Evaluate for malaria.
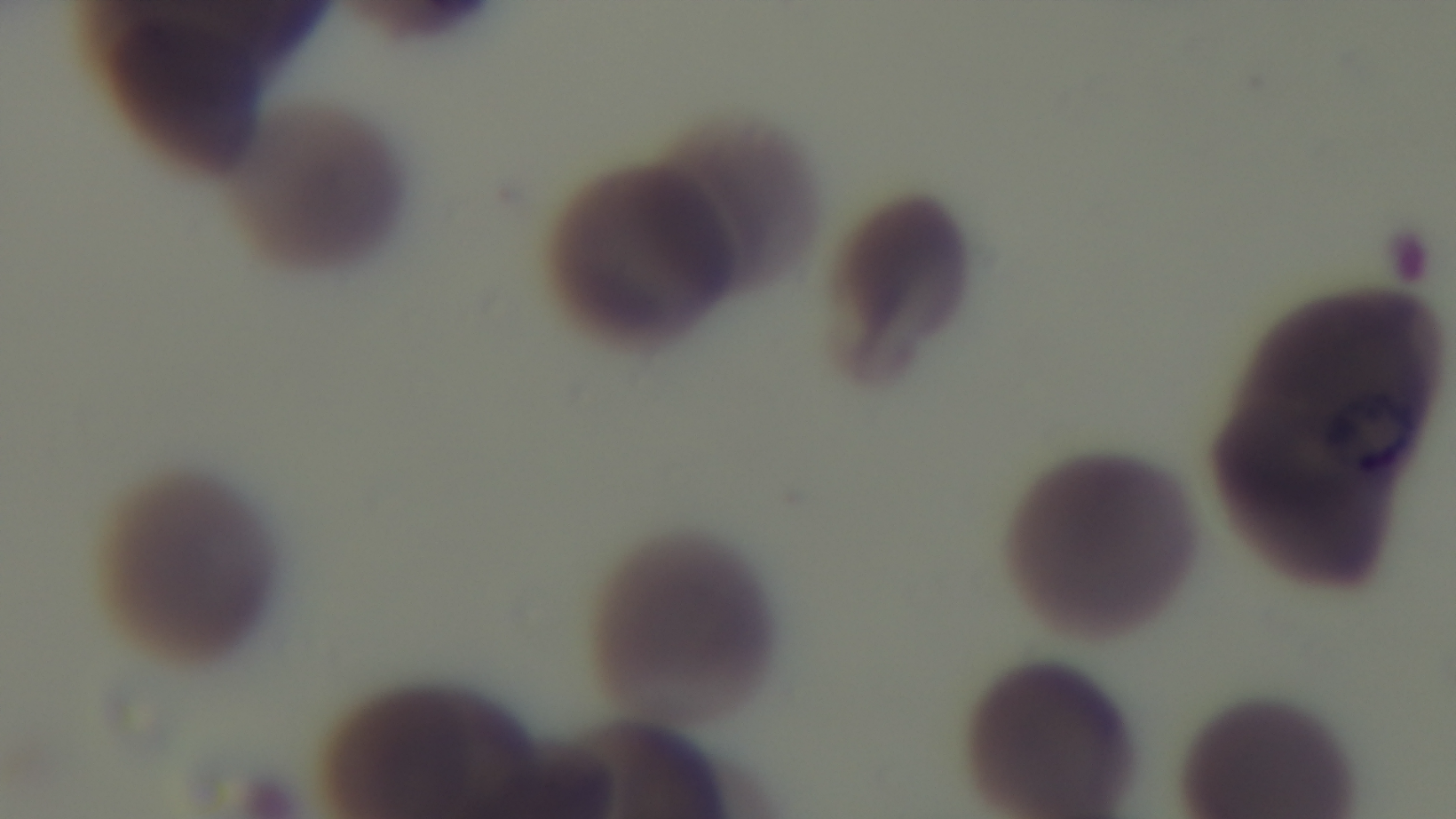
Positive.

{
  "preparation": "thin blood film",
  "stain": "Giemsa",
  "objective": "100x oil immersion",
  "field_of_view": "single",
  "modality": "light microscopy",
  "capture": "mounted 4K digital camera"
}